Assess this cell for malaria.
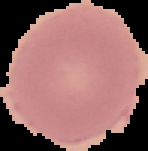

Uninfected.

{
  "image_size": "148×151 pixels",
  "preparation": "thin blood smear",
  "image_type": "segmented cell region with the area outside set to black"
}